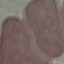
Summary:
  - Malaria status: uninfected
  - Capture: smartphone camera at the microscope eyepiece
  - Stain: Giemsa
  - Image type: automatically extracted cell patch, resized to 64 × 64 pixels
  - Preparation: thin blood smear